Assess for Plasmodium parasites.
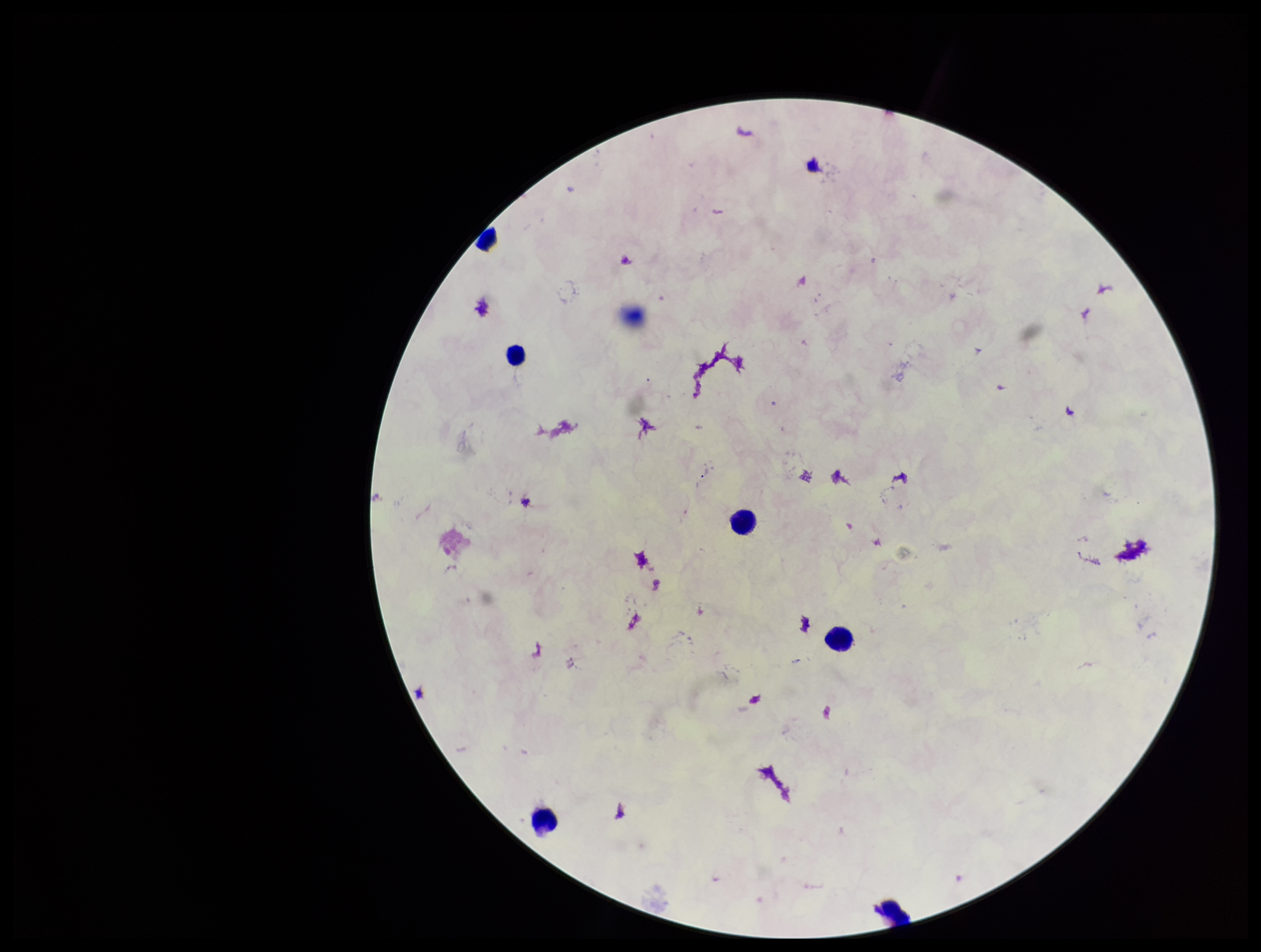

None seen.

parasite_count: 0
preparation: thick smear
field_of_view: single
patient_malaria_status: negative
image_size: 1261×952 pixels
stain: Giemsa
capture: smartphone photograph through the microscope eyepiece
leukocyte_count: 6